State which cell type is depicted.
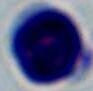

A leukocyte.

magnification = 1000x
modality = micrograph